Comment on the background quality.
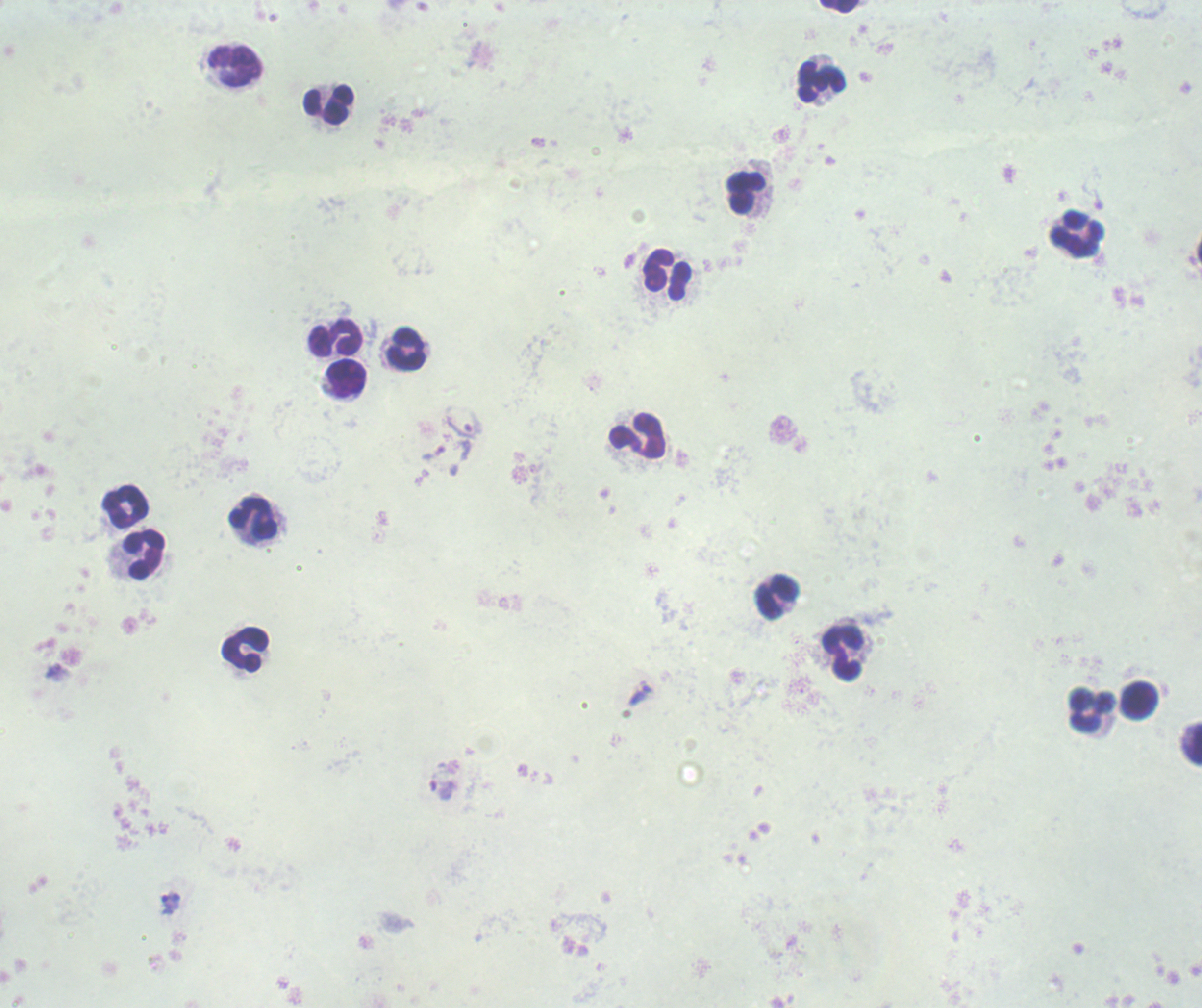
It is poor.

Approximate object centers, in pixels from the top-left corner. Trophozoite locations: (x=464, y=423), (x=433, y=453), (x=639, y=695), (x=442, y=790), (x=169, y=903). Leukocyte locations: (x=840, y=7), (x=821, y=81), (x=328, y=105), (x=745, y=193), (x=1076, y=234), (x=668, y=275), (x=335, y=337), (x=407, y=349), (x=346, y=379), (x=637, y=437), (x=125, y=508), (x=253, y=520), (x=145, y=554), (x=777, y=598), (x=245, y=651), (x=842, y=653), (x=1139, y=700), (x=1092, y=711), (x=1192, y=745). Thick blood film. Previously used in an actual diagnosis. Image is 1202×1008 pixels. Captured at 100x magnification. Romanowsky stain. One field from this slide. Result: Plasmodium parasites detected.